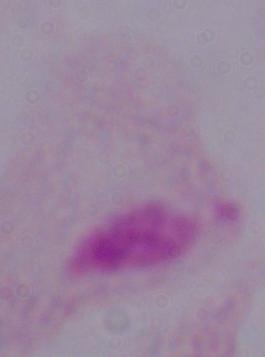

A trichomonad is shown. Photomicrograph. 1000x magnification.